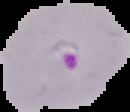

preparation = thin blood smear
image type = segmented cell region with the area outside set to black
image size = 130×112 pixels
malaria status = parasitized